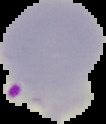
Summary:
  - Image size: 106×124 pixels
  - Preparation: thin blood film
  - Result: Plasmodium parasites identified
  - Image type: segmented cell region on a black background